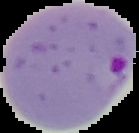
preparation = thin blood smear
result = Plasmodium parasites identified
image type = segmented cell region on a black background
image size = 139×133 pixels